Assess this cell for malaria.
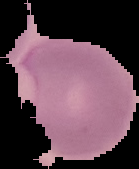
It is parasitized.

image size = 139×169 pixels
image type = cell region segmented out of the field of view; surrounding area masked to black
preparation = thin blood film